Identify the cell.
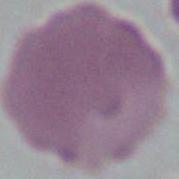
This is an erythrocyte.

Captured at 1000x magnification. Micrograph.